Assess this cell for malaria.
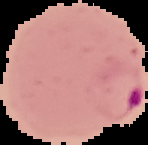

Parasitized.

Image is 148×145 pixels. Cell region segmented out of the field of view; the surrounding area is masked to black. From a thin blood smear.